Identify the parasite.
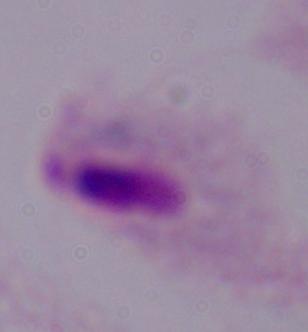
This is a trichomonad.

Summary:
  - Modality: photomicrograph
  - Magnification: 1000x